Locate every Plasmodium parasite.
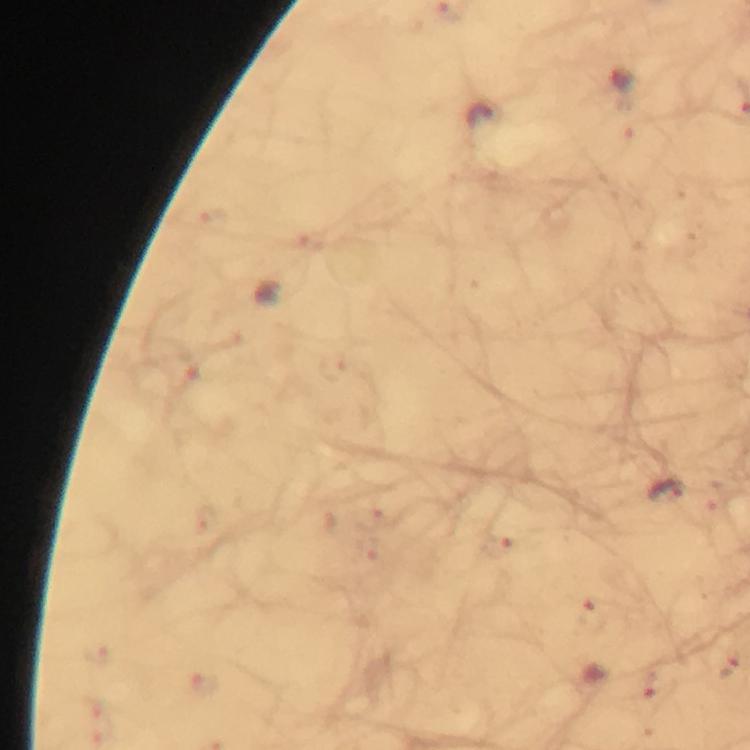

Approximate centers as [x, y] in pixels.
Plasmodium parasites: [667, 492], [498, 545], [729, 664], [650, 683].

Immersion oil applied. At 100x magnification. Thick blood film. Image is 750×750 pixels. Giemsa-stained preparation. From a diagnostic examination for malaria. A crop from one field of view. Photographed through the microscope with a smartphone camera.